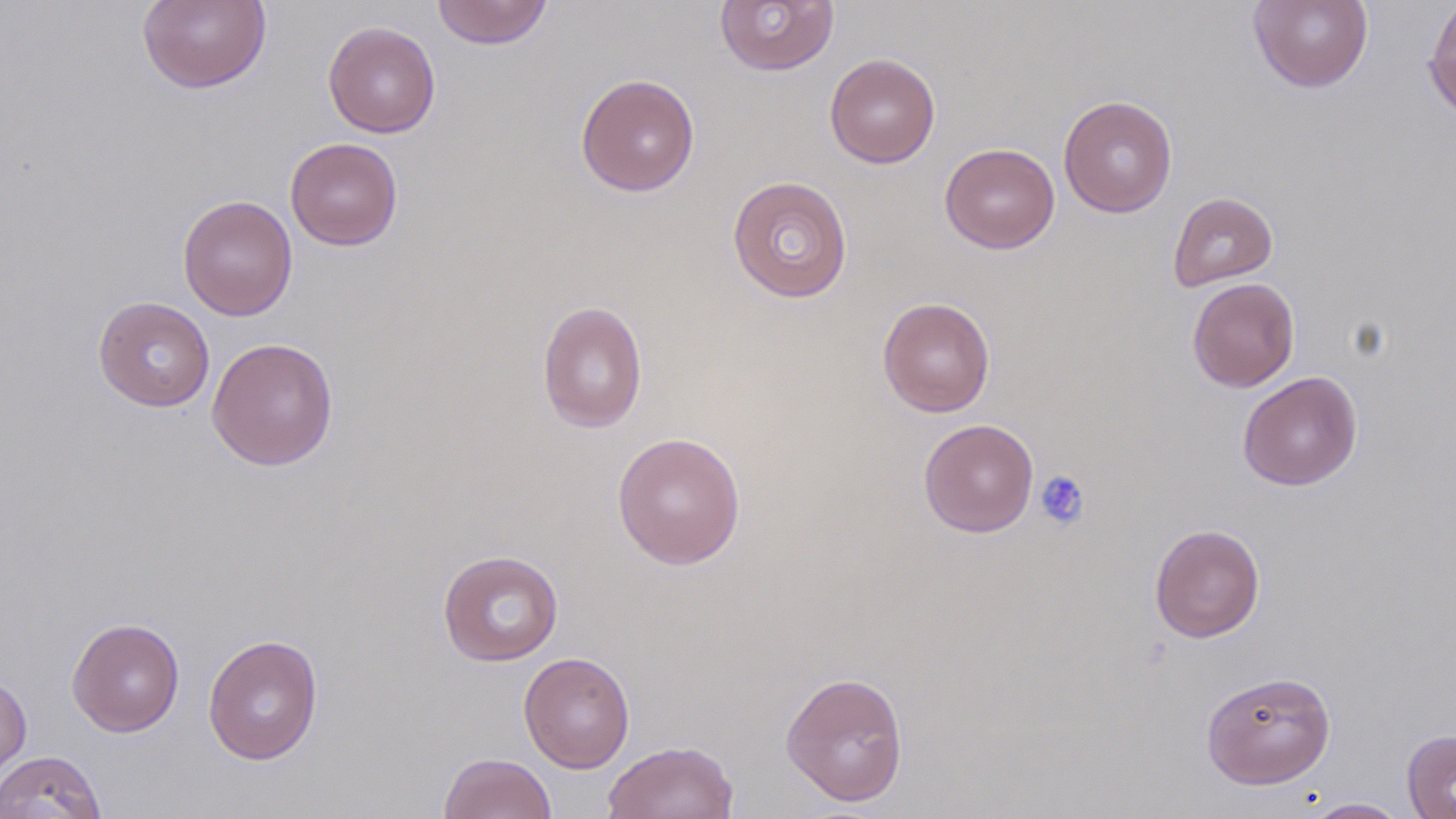
slide-level diagnosis = negative for blood parasites
field of view = one of a larger specimen
modality = optical microscopy
preparation = thin blood film
image size = 1456×819 pixels
magnification = 1000x
uninfected red blood cell locations = approximate bounding boxes as (x1,y1)-(x2,y2) corner pairs in pixels: (137,0)-(272,94), (431,0)-(553,49), (714,0)-(840,76), (1423,0)-(1456,124), (1248,1)-(1374,93), (323,21)-(441,138), (824,52)-(940,169), (576,73)-(700,197), (1058,95)-(1178,217), (285,137)-(403,250), (940,143)-(1060,254), (726,175)-(854,303), (1168,191)-(1278,290), (177,194)-(298,321), (1187,277)-(1300,392), (92,296)-(215,412), (878,297)-(995,417), (536,300)-(648,433), (206,337)-(338,471), (1237,371)-(1363,491), (918,418)-(1039,537), (612,432)-(746,570), (1149,523)-(1265,643), (437,549)-(564,666), (66,617)-(185,737), (202,633)-(324,765), (518,652)-(635,772), (1201,670)-(1336,789), (780,671)-(909,807), (0,672)-(32,787), (1402,729)-(1456,819), (602,740)-(739,819), (0,750)-(107,819), (438,752)-(557,819), (1301,798)-(1408,818)
platelet locations = approximate bounding boxes as (x1,y1)-(x2,y2) corner pairs in pixels: (1035,470)-(1090,530)
stain = May-Grünwald-Giemsa